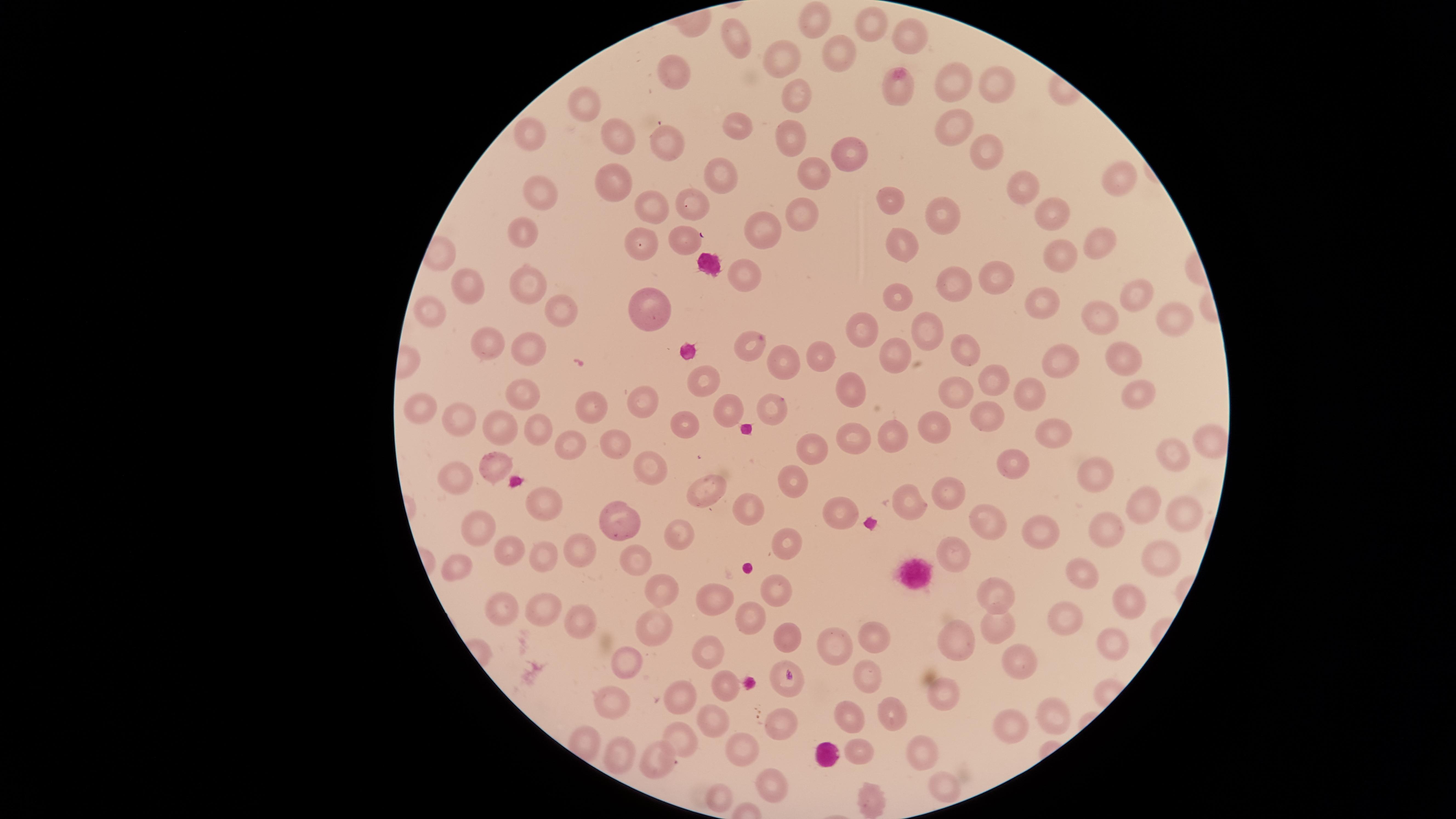
Approximate marker points as [x, y] in pixels. Uninfected RBCs: [819, 20], [871, 20], [913, 35], [731, 36], [786, 56], [841, 56], [682, 76], [955, 85], [1001, 87], [893, 91], [799, 97], [589, 101], [958, 121], [734, 125], [668, 130], [788, 131], [527, 140], [616, 146], [985, 147], [842, 154], [815, 170], [723, 176], [1115, 177], [538, 182], [612, 183], [1026, 189], [694, 201], [890, 201], [656, 208], [1046, 211], [942, 216], [805, 218], [759, 228], [525, 234], [682, 234], [639, 244], [1093, 245], [899, 248], [1052, 250], [743, 276], [985, 278], [959, 280], [532, 284], [472, 293], [900, 293], [1134, 296], [1042, 301], [558, 306], [1166, 310], [645, 313], [436, 320], [1108, 322], [857, 326], [923, 332], [749, 343], [488, 346], [531, 351], [819, 351], [897, 351], [967, 352], [783, 358], [1056, 358], [1118, 358], [993, 379], [707, 382], [857, 387], [959, 389], [1031, 391], [521, 394], [1134, 395], [646, 397], [774, 401], [589, 407], [421, 408], [728, 412], [987, 413], [463, 418], [532, 425], [937, 425], [688, 427], [495, 431], [1046, 432], [896, 435], [611, 436], [854, 437], [571, 441], [1210, 441], [809, 447], [1174, 460], [495, 467], [646, 467], [1011, 467], [1099, 470], [453, 472], [706, 479], [792, 480], [945, 485], [551, 501], [911, 501], [1143, 505], [747, 508], [842, 513], [1170, 513], [625, 519], [991, 525], [1104, 526], [675, 527], [474, 529], [1050, 534], [790, 543], [635, 548], [505, 549], [583, 549], [952, 551], [1160, 557], [546, 559], [456, 562], [1078, 576], [779, 586], [664, 589], [992, 596], [708, 601], [1127, 601], [506, 611], [546, 611], [755, 615], [1060, 616], [579, 625], [997, 627], [662, 629], [786, 634], [874, 634], [949, 639], [836, 644], [1117, 644], [708, 652], [625, 658], [1016, 662], [868, 671], [785, 684], [944, 686], [690, 694], [722, 694], [615, 697], [889, 711], [850, 713], [1054, 713], [782, 715], [708, 721], [1014, 724], [683, 740], [858, 748], [918, 749], [738, 753], [620, 754], [655, 763], [770, 780], [946, 785], [721, 797], [881, 798]. One field of view of the specimen. Giemsa-stained preparation. Thin smear of blood. Smartphone photograph through the microscope eyepiece. Presence: no malaria parasites identified. The visible region is circular. Image is 1456×819 pixels.